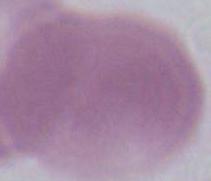

modality: micrograph
magnification: 1000x
identification: erythrocyte